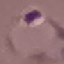

Summary:
  - Result: malaria parasites detected
  - Image type: automatically extracted cell patch, resized to 64 × 64 pixels
  - Preparation: thin blood film
  - Stain: Giemsa
  - Capture: smartphone camera at the microscope eyepiece